Locate every blood parasite and identify its species.
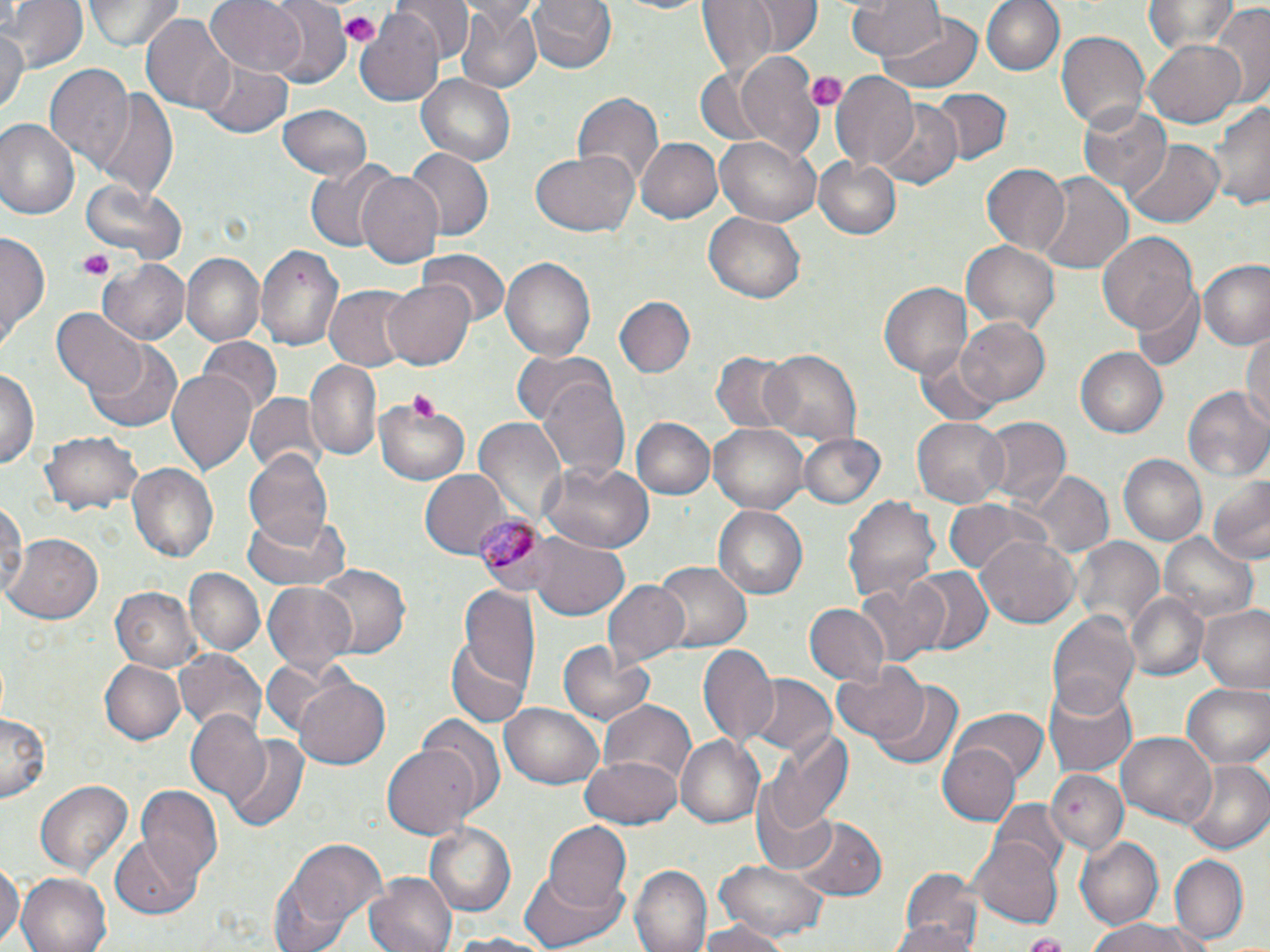
Approximate bounding boxes as (x1,y1)-(x2,y2) corner pairs in pixels.
Plasmodium malariae-infected red blood cells: (476,511)-(553,595).
No Plasmodium falciparum, Plasmodium ovale, Plasmodium vivax, Babesia divergens, or Trypanosoma brucei observed.

Uninfected red blood cell locations: (3,0)-(85,72), (83,0)-(182,52), (204,0)-(308,78), (264,0)-(352,89), (397,0)-(473,68), (526,0)-(616,77), (599,0)-(717,16), (695,0)-(781,81), (742,0)-(820,56), (845,0)-(945,63), (981,0)-(1065,77), (1146,0)-(1239,55), (454,1)-(541,93), (1207,5)-(1270,107), (355,9)-(445,105), (139,10)-(233,113), (877,11)-(982,92), (0,27)-(26,119), (1056,30)-(1149,130), (1145,35)-(1245,126), (739,55)-(827,161), (198,56)-(295,138), (43,65)-(133,171), (832,73)-(920,170), (418,75)-(515,164), (929,88)-(1011,164), (92,91)-(177,202), (573,92)-(663,188), (1207,92)-(1270,212), (1076,100)-(1172,198), (879,103)-(960,187), (277,105)-(373,182), (0,119)-(79,222), (636,137)-(722,224), (714,137)-(820,225), (1123,140)-(1223,227), (406,150)-(492,241), (531,151)-(638,239), (815,155)-(903,239), (305,163)-(395,251), (980,163)-(1069,255), (356,171)-(445,269), (1036,171)-(1132,273), (81,178)-(183,264), (704,212)-(805,304), (0,230)-(49,349), (1096,231)-(1197,339), (961,237)-(1060,336), (257,245)-(341,348), (420,248)-(508,325), (183,254)-(263,344), (500,257)-(595,362), (99,260)-(190,344), (1200,262)-(1270,350), (385,278)-(475,370), (879,282)-(974,380), (1130,284)-(1205,371), (325,287)-(415,371), (614,295)-(698,376), (53,309)-(148,398), (957,316)-(1050,407), (1242,331)-(1269,428), (198,337)-(281,418), (84,341)-(182,432), (1074,347)-(1168,439), (915,349)-(1006,428), (760,350)-(861,445), (708,351)-(794,436), (513,352)-(612,427), (304,360)-(382,463), (0,366)-(39,469), (168,368)-(258,478), (537,374)-(631,480), (1184,387)-(1270,482), (245,394)-(320,473), (374,400)-(469,483), (912,414)-(1009,505), (975,416)-(1069,509), (630,418)-(716,500), (472,419)-(566,528), (709,422)-(811,513), (38,431)-(139,515), (795,431)-(886,509), (244,451)-(335,548), (1119,455)-(1207,546), (539,460)-(653,555), (126,461)-(220,563), (1030,471)-(1113,560), (421,472)-(511,557), (1208,473)-(1270,564), (841,492)-(941,606), (0,495)-(27,604), (945,499)-(1050,577), (712,504)-(810,601), (240,508)-(348,593), (975,533)-(1079,627), (529,534)-(630,619), (1161,534)-(1258,622), (7,535)-(104,623), (1071,536)-(1163,636), (655,563)-(749,654), (312,564)-(410,661), (904,566)-(992,658), (185,568)-(265,655), (602,580)-(690,667), (855,580)-(945,667), (263,582)-(358,675), (111,586)-(203,671), (457,589)-(542,692), (1124,592)-(1210,682), (804,604)-(891,688), (1198,605)-(1269,693), (1047,607)-(1140,721), (445,631)-(534,727), (557,640)-(658,728), (698,645)-(779,744), (173,648)-(267,735), (101,661)-(184,744), (832,664)-(930,744), (743,675)-(835,758), (292,677)-(392,770), (868,677)-(964,770), (1044,681)-(1137,778), (1182,683)-(1269,768), (600,701)-(697,789), (501,705)-(601,789), (951,707)-(1050,783), (0,712)-(48,805), (185,712)-(272,804), (419,718)-(506,818), (759,725)-(853,840), (1116,730)-(1217,825), (224,737)-(309,832), (676,737)-(765,829), (384,741)-(481,839), (939,745)-(1021,825), (581,754)-(684,828), (1182,759)-(1270,854), (1049,771)-(1125,854), (35,778)-(135,877), (137,788)-(225,884), (752,799)-(838,878), (988,800)-(1067,875), (789,818)-(885,900), (542,822)-(632,913), (424,823)-(516,917), (267,837)-(388,951), (1075,837)-(1163,929), (110,838)-(201,918), (971,838)-(1064,927), (1169,856)-(1249,943), (0,857)-(20,949), (715,859)-(830,942), (632,867)-(709,952), (519,869)-(627,951), (897,871)-(984,951), (365,872)-(458,952), (16,873)-(111,952), (889,916)-(977,952), (696,919)-(791,952), (1088,919)-(1210,952), (442,931)-(560,951), (1018,937)-(1071,949). Platelet locations: (338,13)-(382,45), (806,70)-(847,112), (77,251)-(113,281). Slide-level diagnosis: Plasmodium malariae. Light microscopy. Single field of view. Thin blood smear. Image is 1270×952 pixels. Captured at 1000x magnification. May-Grünwald-Giemsa stain.